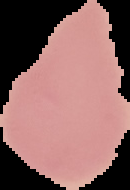
Result: negative for malaria parasites. From a thin blood film. Image is 130×190 pixels. Segmented cell region on a black background.